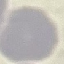

Result: negative for malaria parasites. Photographed with a smartphone camera at the microscope eyepiece. Automatically extracted cell patch, resized to 64 × 64 pixels. Thin blood film. Giemsa-stained preparation.